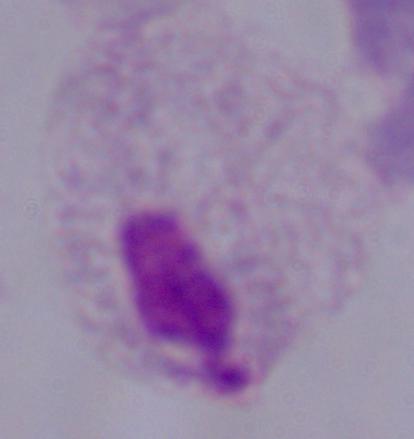 A trichomonad is shown. Captured at 1000x magnification. Photomicrograph.